Identify the preparation type.
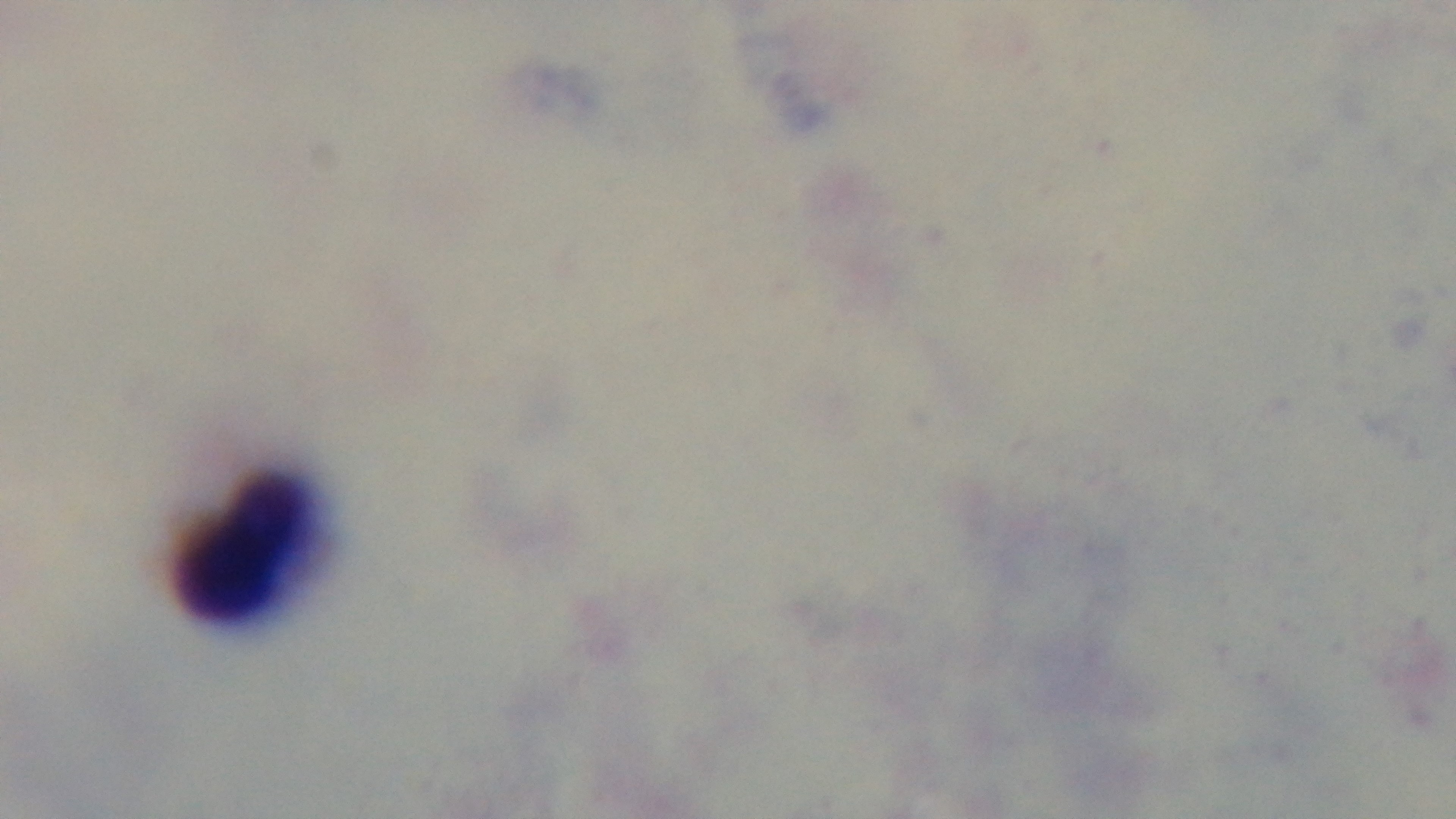

Thick.

Summary:
  - Modality: light microscopy
  - Field of view: one from the slide
  - Capture: mounted 4K digital camera
  - Objective: 100x oil immersion
  - Malaria status: uninfected
  - Stain: Giemsa